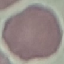
malaria status = uninfected
image type = automatically extracted cell patch, resized to 64 × 64 pixels
stain = Giemsa
preparation = thin blood smear
capture = smartphone camera at the microscope eyepiece